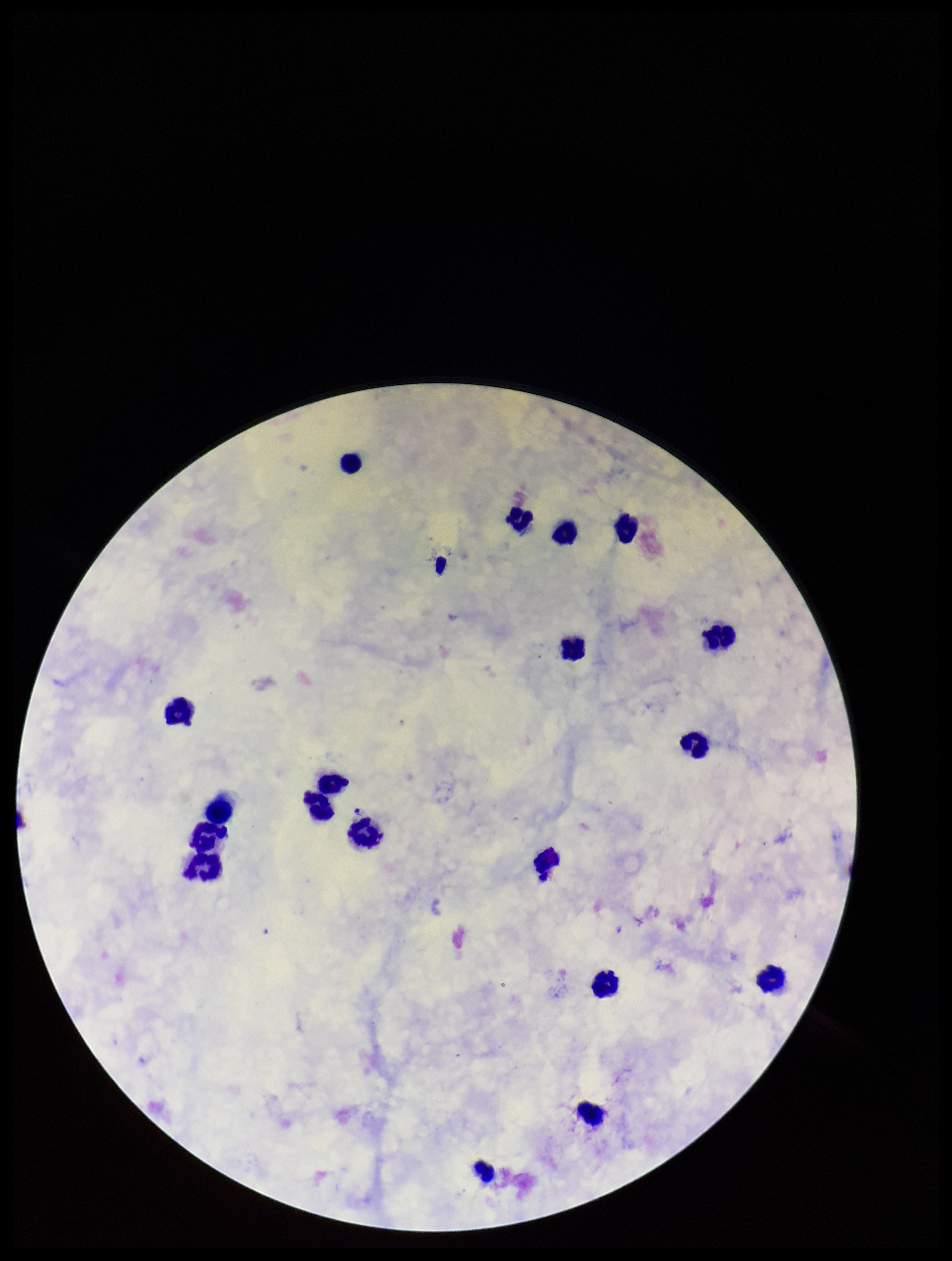

Patient malaria status: positive. Plasmodium parasites: none identified. Preparation: thick. Species reported for this patient: Plasmodium falciparum. Image is 952×1261 pixels. Stained with Giemsa. Leukocyte count: 19. Parasite count: 0. Photographed through the microscope eyepiece with a smartphone camera. Single field of view.